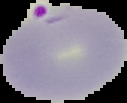
Segmented cell region on a black background. From a thin blood smear. Result: malaria parasites identified. Image is 127×103 pixels.